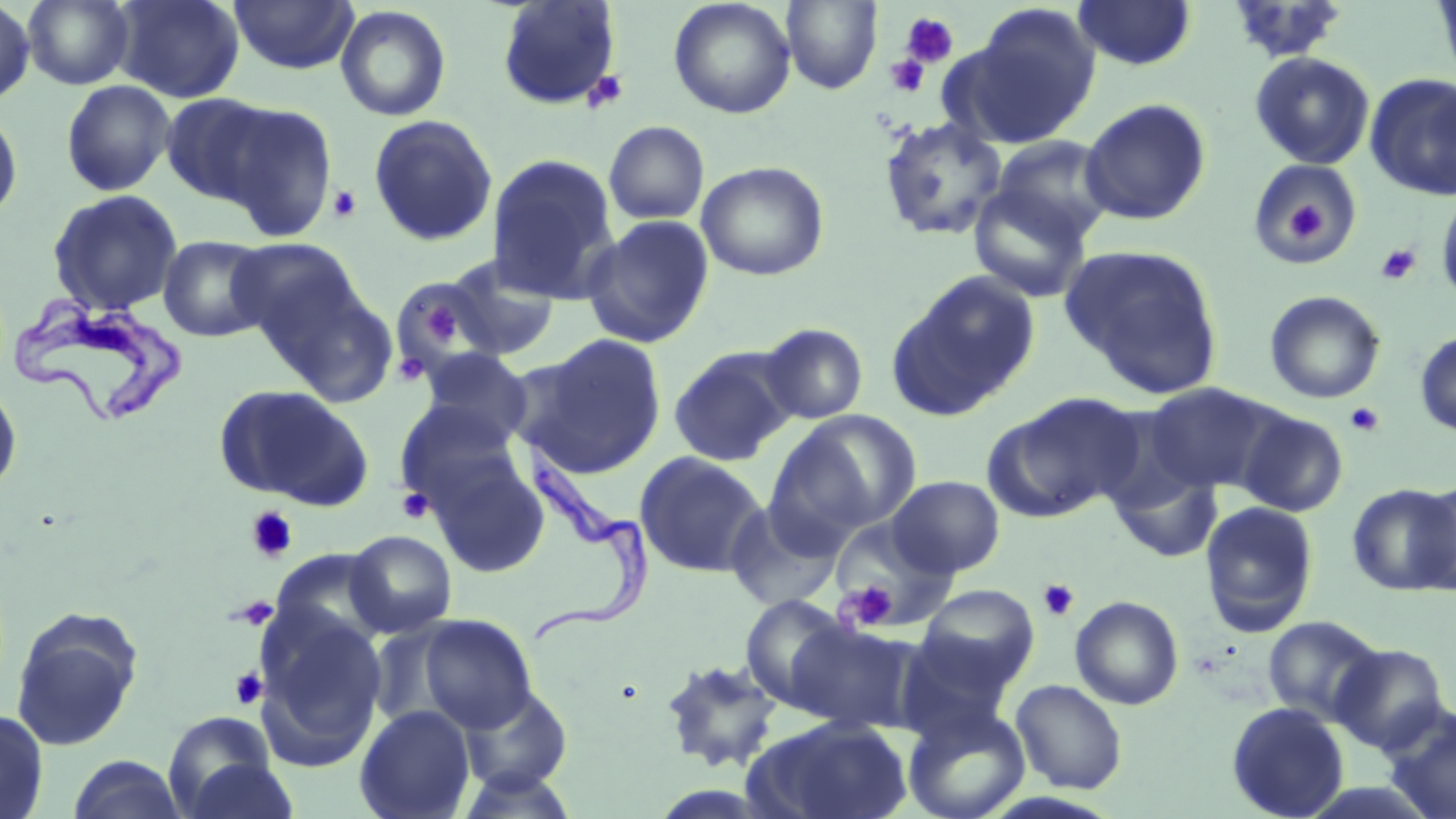
Approximate bounding boxes as named x1/y1/x2/y2 corners in pixels. Uninfected red blood cell locations: (x1=22, y1=0, x2=135, y2=89), (x1=112, y1=0, x2=245, y2=103), (x1=229, y1=0, x2=359, y2=75), (x1=668, y1=0, x2=796, y2=119), (x1=1073, y1=0, x2=1197, y2=70), (x1=1431, y1=0, x2=1456, y2=87), (x1=0, y1=1, x2=36, y2=106), (x1=496, y1=1, x2=622, y2=111), (x1=782, y1=1, x2=882, y2=93), (x1=1224, y1=1, x2=1352, y2=65), (x1=966, y1=3, x2=1101, y2=141), (x1=334, y1=5, x2=452, y2=122), (x1=1249, y1=51, x2=1376, y2=169), (x1=1365, y1=74, x2=1456, y2=200), (x1=60, y1=79, x2=176, y2=196), (x1=160, y1=92, x2=279, y2=206), (x1=1080, y1=97, x2=1212, y2=225), (x1=212, y1=100, x2=338, y2=241), (x1=0, y1=101, x2=23, y2=224), (x1=367, y1=114, x2=498, y2=248), (x1=879, y1=116, x2=1008, y2=241), (x1=603, y1=120, x2=710, y2=224), (x1=990, y1=135, x2=1117, y2=244), (x1=486, y1=153, x2=621, y2=304), (x1=1246, y1=157, x2=1363, y2=265), (x1=696, y1=160, x2=830, y2=281), (x1=968, y1=185, x2=1092, y2=303), (x1=1436, y1=187, x2=1456, y2=311), (x1=47, y1=188, x2=184, y2=316), (x1=581, y1=215, x2=715, y2=348), (x1=157, y1=234, x2=274, y2=342), (x1=229, y1=236, x2=363, y2=350), (x1=1063, y1=244, x2=1225, y2=397), (x1=439, y1=254, x2=561, y2=362), (x1=890, y1=270, x2=1041, y2=418), (x1=264, y1=275, x2=401, y2=409), (x1=399, y1=279, x2=480, y2=366), (x1=1264, y1=290, x2=1385, y2=404), (x1=758, y1=323, x2=868, y2=424), (x1=1414, y1=329, x2=1456, y2=437), (x1=524, y1=334, x2=668, y2=476), (x1=668, y1=346, x2=796, y2=467), (x1=420, y1=348, x2=533, y2=448), (x1=0, y1=379, x2=22, y2=497), (x1=1145, y1=383, x2=1280, y2=495), (x1=215, y1=384, x2=373, y2=509), (x1=989, y1=393, x2=1143, y2=519), (x1=393, y1=400, x2=523, y2=510), (x1=779, y1=409, x2=923, y2=533), (x1=1237, y1=409, x2=1349, y2=516), (x1=423, y1=447, x2=551, y2=578), (x1=634, y1=451, x2=768, y2=578), (x1=1110, y1=461, x2=1223, y2=564), (x1=886, y1=476, x2=1006, y2=577), (x1=1412, y1=481, x2=1456, y2=595), (x1=1346, y1=483, x2=1456, y2=596), (x1=725, y1=500, x2=846, y2=612), (x1=1200, y1=501, x2=1319, y2=636), (x1=831, y1=519, x2=959, y2=633), (x1=345, y1=530, x2=458, y2=637), (x1=917, y1=584, x2=1040, y2=690), (x1=740, y1=594, x2=854, y2=711), (x1=1070, y1=596, x2=1184, y2=710), (x1=10, y1=607, x2=144, y2=751), (x1=253, y1=608, x2=387, y2=768), (x1=415, y1=614, x2=537, y2=732), (x1=1262, y1=615, x2=1384, y2=725), (x1=786, y1=621, x2=917, y2=732), (x1=896, y1=632, x2=1017, y2=740), (x1=1330, y1=643, x2=1449, y2=753), (x1=658, y1=657, x2=785, y2=773), (x1=1010, y1=680, x2=1128, y2=794), (x1=457, y1=684, x2=575, y2=796), (x1=1225, y1=701, x2=1350, y2=819), (x1=1381, y1=703, x2=1456, y2=819), (x1=354, y1=705, x2=476, y2=819), (x1=903, y1=705, x2=1030, y2=819), (x1=0, y1=707, x2=49, y2=819), (x1=162, y1=712, x2=282, y2=817), (x1=748, y1=716, x2=913, y2=819), (x1=67, y1=754, x2=188, y2=819), (x1=180, y1=757, x2=302, y2=818). Platelet locations: (x1=900, y1=12, x2=959, y2=69), (x1=885, y1=54, x2=930, y2=97), (x1=582, y1=69, x2=629, y2=113), (x1=328, y1=185, x2=363, y2=222), (x1=1280, y1=192, x2=1331, y2=249), (x1=1376, y1=243, x2=1422, y2=285), (x1=419, y1=299, x2=461, y2=347), (x1=394, y1=351, x2=430, y2=385), (x1=1345, y1=402, x2=1385, y2=437), (x1=396, y1=488, x2=434, y2=524), (x1=245, y1=506, x2=299, y2=563), (x1=1038, y1=579, x2=1079, y2=621), (x1=839, y1=582, x2=899, y2=631), (x1=231, y1=596, x2=278, y2=630), (x1=229, y1=666, x2=268, y2=711). Trypanosoma brucei locations: (x1=10, y1=290, x2=186, y2=425), (x1=512, y1=439, x2=650, y2=644). Slide-level diagnosis: Trypanosoma brucei. Thin blood film. Image is 1456×819 pixels. Single field of view. Captured at 1000x magnification. Optical microscopy. May-Grünwald-Giemsa stain.